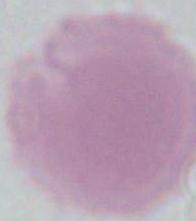
modality = micrograph
magnification = 1000x
identification = erythrocyte